Identify the blood parasite species.
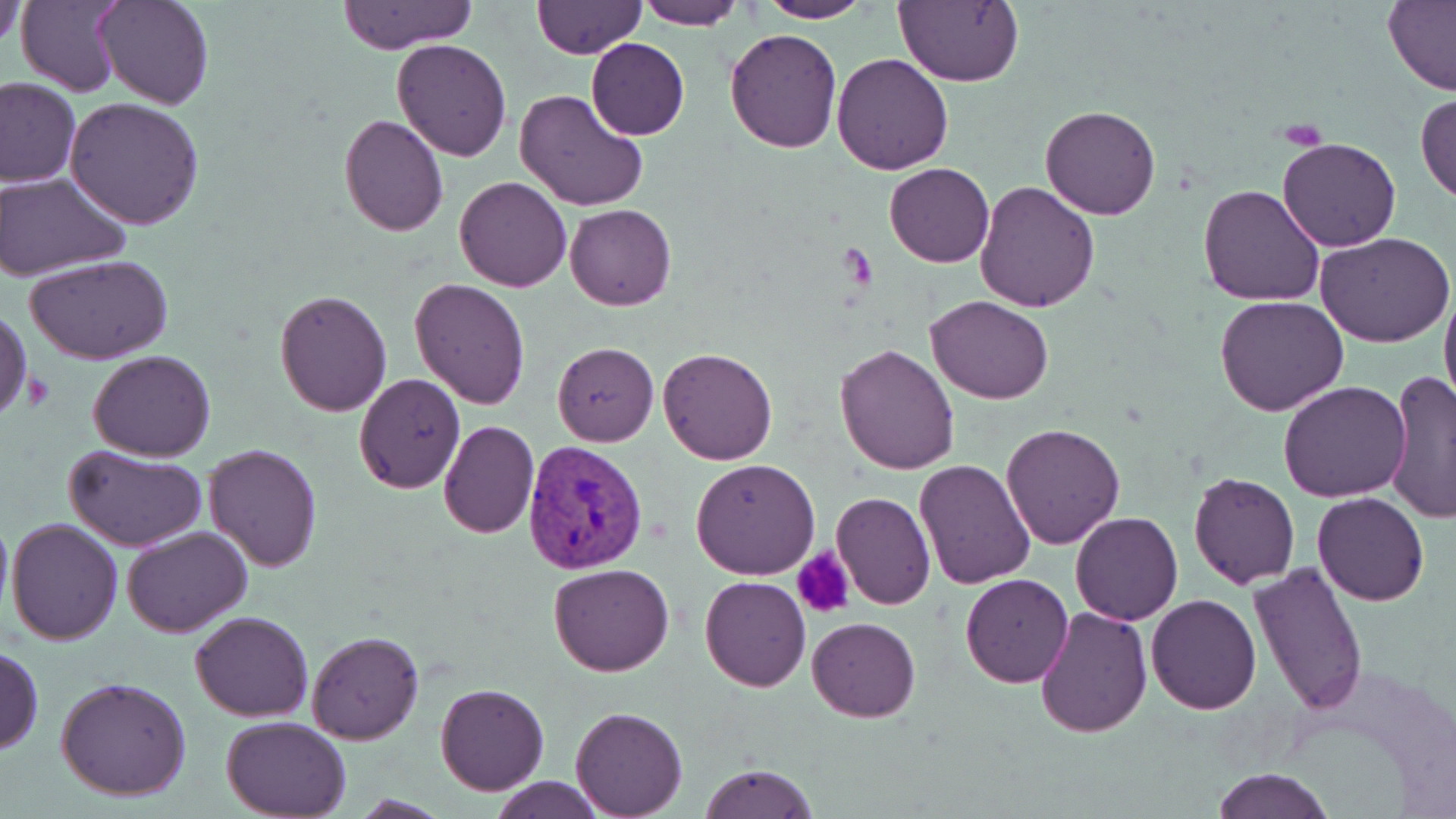

Plasmodium vivax.

Approximate bounding boxes as [x1, y1, x2, y2] in pixels. Plasmodium vivax-infected red blood cell locations: [523, 440, 649, 576]. Uninfected red blood cell locations: [18, 0, 127, 98], [95, 0, 214, 111], [338, 0, 479, 52], [758, 0, 871, 24], [894, 0, 1022, 87], [2, 1, 27, 53], [532, 1, 645, 59], [631, 1, 744, 28], [1382, 1, 1456, 95], [724, 27, 843, 153], [586, 38, 690, 140], [390, 39, 513, 161], [831, 52, 956, 174], [0, 77, 80, 186], [514, 88, 649, 214], [1416, 92, 1456, 203], [65, 97, 204, 230], [1040, 103, 1163, 220], [338, 114, 449, 237], [1278, 137, 1401, 253], [885, 163, 994, 267], [1, 172, 129, 280], [455, 176, 572, 291], [974, 181, 1100, 313], [1197, 183, 1327, 307], [565, 204, 676, 311], [1317, 231, 1453, 347], [27, 253, 174, 365], [409, 277, 528, 410], [1439, 286, 1455, 416], [275, 289, 391, 415], [926, 296, 1054, 403], [1215, 296, 1348, 417], [0, 304, 32, 426], [552, 341, 658, 446], [834, 343, 960, 474], [658, 346, 777, 465], [89, 349, 217, 460], [1382, 371, 1454, 522], [354, 374, 465, 492], [1278, 381, 1411, 502], [437, 421, 539, 539], [1001, 424, 1125, 549], [64, 444, 207, 552], [204, 444, 322, 571], [690, 459, 820, 578], [915, 460, 1036, 589], [1187, 469, 1301, 589], [831, 491, 936, 610], [1312, 492, 1430, 607], [1070, 513, 1182, 625], [5, 517, 123, 645], [122, 525, 254, 638], [1247, 562, 1367, 716], [547, 563, 675, 678], [959, 573, 1073, 688], [700, 576, 811, 692], [1147, 593, 1263, 714], [1036, 605, 1152, 739], [189, 611, 314, 721], [808, 617, 920, 722], [306, 630, 424, 745], [1, 645, 44, 754], [56, 676, 191, 802], [435, 684, 548, 795], [569, 705, 688, 817], [220, 715, 351, 819], [698, 764, 817, 819], [1212, 768, 1336, 819], [487, 777, 608, 817]. Platelet locations: [793, 549, 855, 620]. May-Grünwald-Giemsa stain. Thin blood smear. Optical microscopy. One field of a larger specimen. Image is 1456×819 pixels. Captured at 1000x magnification.